Classify this cell by malaria status.
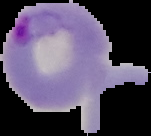

Parasitized.

preparation: thin blood film
image_size: 151×136 pixels
image_type: segmented cell region with the area outside set to black